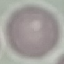
result = no malaria parasites detected
capture = smartphone camera at the microscope eyepiece
preparation = thin blood film
stain = Giemsa
image type = cell patch, automatically extracted from a larger field of view and resized to 64 × 64 pixels